Assess this cell for malaria.
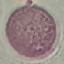

It is uninfected.

Giemsa stain. Thin blood smear. Automatically extracted cell patch, resized to 64 × 64 pixels. Photographed with a smartphone camera at the microscope eyepiece.